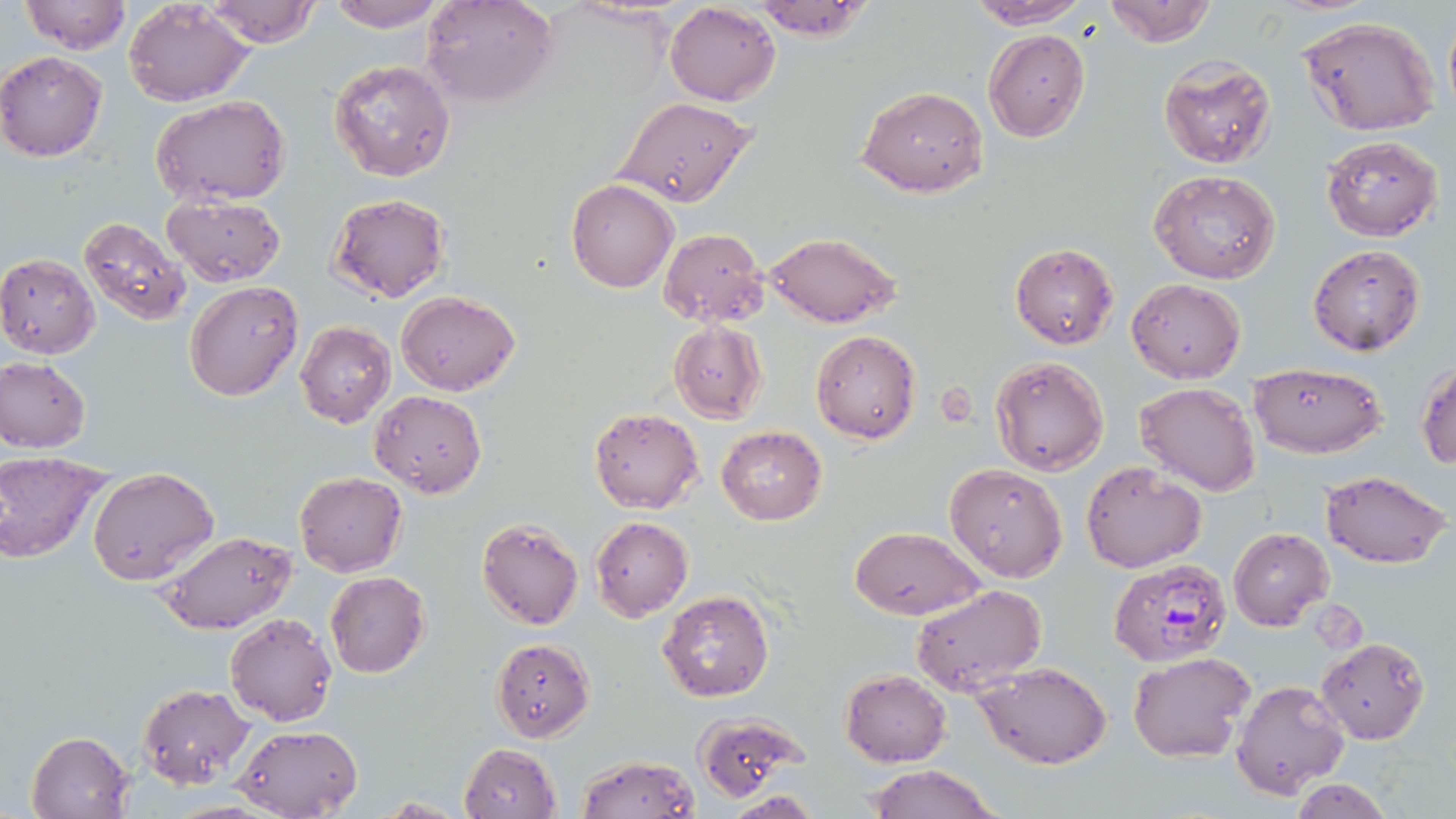

slide_level_diagnosis: Plasmodium falciparum
image_size: 1456×819 pixels
plasmodium_falciparum_infected_red_blood_cell_locations: 'approximate bounding boxes as [x1, y1, x2, y2] in pixels: [1108, 559, 1231, 667]'
magnification: 1000x
uninfected_red_blood_cell_locations: 'approximate bounding boxes as [x1, y1, x2, y2] in pixels: [203, 0, 323, 48], [422, 0, 557, 108], [749, 0, 876, 41], [965, 0, 1092, 29], [1102, 0, 1218, 47], [21, 1, 132, 54], [122, 1, 255, 106], [322, 1, 450, 32], [664, 2, 781, 106], [1443, 5, 1456, 125], [1296, 15, 1443, 136], [983, 29, 1090, 142], [0, 51, 107, 162], [1159, 56, 1277, 169], [329, 59, 457, 184], [858, 86, 988, 197], [151, 94, 291, 206], [613, 95, 756, 208], [1320, 134, 1443, 241], [1149, 169, 1281, 285], [568, 179, 676, 293], [161, 193, 286, 287], [327, 193, 450, 303], [78, 216, 191, 325], [658, 228, 768, 327], [763, 230, 900, 328], [1011, 243, 1119, 349], [1307, 244, 1427, 355], [0, 253, 100, 358], [1126, 278, 1247, 383], [185, 281, 304, 403], [397, 290, 519, 396], [295, 320, 396, 428], [669, 321, 767, 424], [811, 329, 921, 444], [990, 355, 1110, 476], [0, 357, 90, 452], [1415, 361, 1456, 471], [1248, 362, 1388, 457], [1133, 382, 1260, 497], [369, 390, 486, 496], [589, 407, 705, 513], [716, 425, 826, 525], [0, 452, 112, 563], [1081, 462, 1206, 573], [945, 464, 1068, 581], [88, 466, 219, 586], [1321, 469, 1452, 568], [294, 472, 406, 576], [590, 516, 693, 621], [476, 519, 583, 630], [850, 526, 986, 621], [1228, 528, 1333, 630], [159, 530, 296, 635], [324, 572, 431, 677], [911, 583, 1047, 696], [658, 590, 775, 703], [224, 612, 338, 727], [1316, 637, 1431, 744], [490, 638, 595, 741], [1127, 651, 1256, 763], [976, 661, 1113, 768], [839, 669, 950, 766], [1231, 679, 1351, 798], [137, 684, 254, 787], [694, 711, 806, 801], [233, 724, 364, 817], [26, 730, 133, 819], [459, 743, 561, 819], [578, 754, 700, 819], [863, 763, 1002, 819], [1287, 776, 1396, 819], [721, 791, 820, 818], [373, 795, 472, 816]'
field_of_view: one of a larger specimen
modality: light microscopy
preparation: thin blood smear
stain: May-Grünwald-Giemsa